Identify the cell.
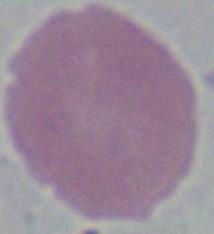
An erythrocyte.

Summary:
  - Modality: micrograph
  - Magnification: 1000x